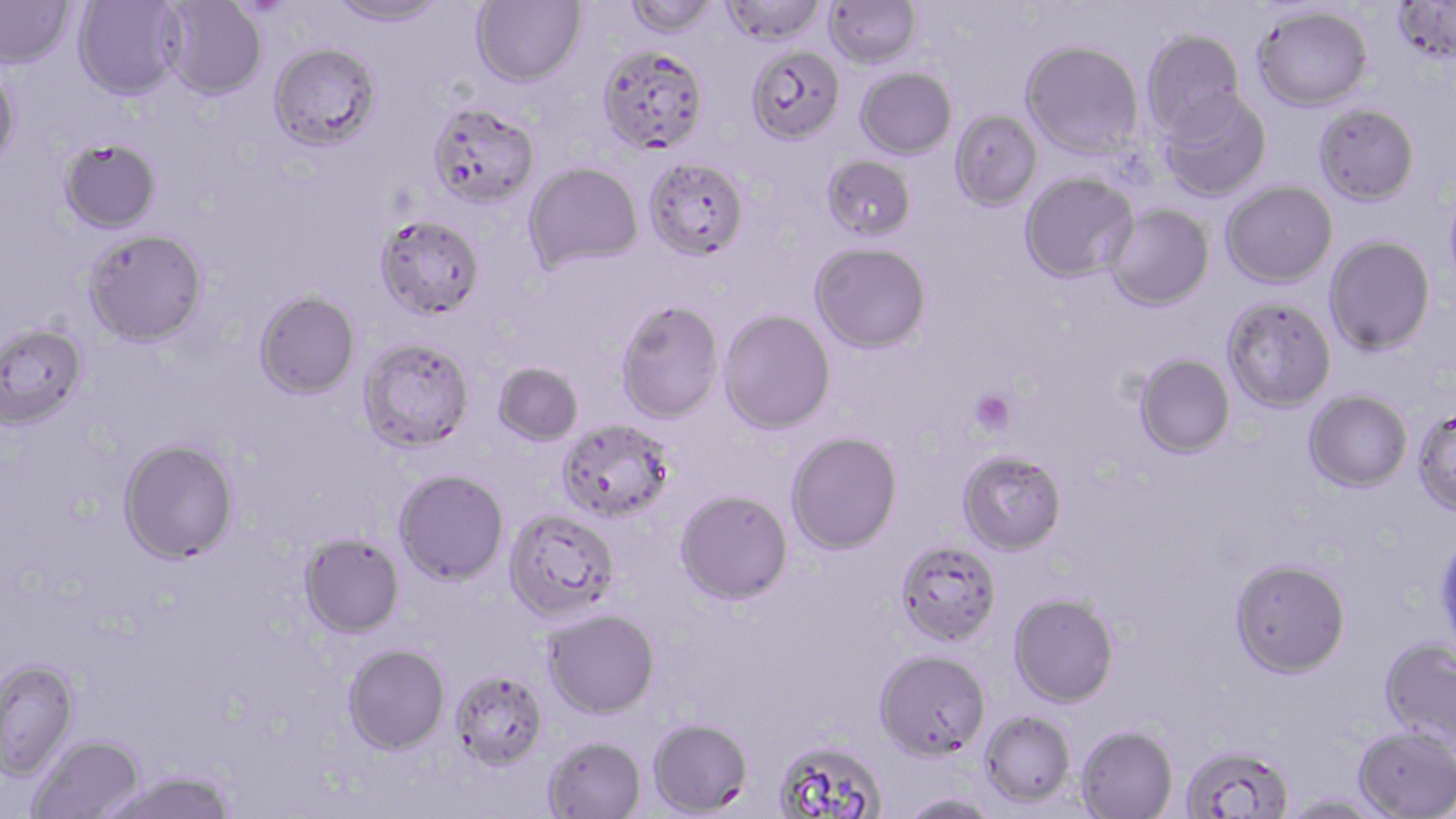
Summary:
  - Coordinate format: approximate bounding boxes as (x1,y1)-(x2,y2) corner pairs in pixels
  - Uninfected red blood cell locations: (0,0)-(74,69), (73,0)-(184,100), (327,0)-(451,27), (470,0)-(586,86), (623,0)-(720,37), (720,0)-(827,45), (823,0)-(921,68), (1392,0)-(1456,65), (160,1)-(267,99), (1252,5)-(1373,111), (1141,30)-(1246,138), (1020,40)-(1144,157), (269,42)-(381,150), (597,44)-(709,154), (746,45)-(845,145), (0,65)-(22,171), (855,67)-(957,159), (1157,88)-(1272,201), (427,102)-(540,209), (1314,104)-(1420,205), (949,110)-(1042,211), (59,137)-(162,233), (821,155)-(917,242), (644,156)-(749,261), (524,161)-(643,273), (1019,172)-(1139,283), (1221,181)-(1337,288), (1444,181)-(1456,296), (1104,204)-(1215,310), (375,213)-(485,320), (82,229)-(208,348), (1324,235)-(1436,355), (810,241)-(931,353), (254,291)-(360,400), (1222,297)-(1336,413), (615,300)-(724,423), (719,310)-(836,434), (0,322)-(88,431), (357,338)-(474,454), (1134,354)-(1235,458), (492,362)-(584,446), (1304,390)-(1412,492), (1412,408)-(1456,516), (557,419)-(676,524), (785,431)-(902,555), (118,438)-(240,564), (957,450)-(1067,554), (393,469)-(509,585), (675,490)-(793,604), (504,508)-(620,623), (1435,526)-(1456,661), (298,533)-(405,638), (896,540)-(1003,646), (1229,558)-(1351,677), (1008,592)-(1119,707), (543,609)-(660,719), (1379,637)-(1456,748), (343,644)-(450,755), (874,648)-(991,760), (0,660)-(80,782), (448,669)-(548,770), (980,710)-(1076,807), (648,718)-(753,816), (1076,725)-(1178,818), (1353,726)-(1456,818), (29,735)-(146,818), (543,735)-(646,818), (774,740)-(887,819), (1179,743)-(1293,819), (101,772)-(237,819), (900,793)-(1004,819), (1281,795)-(1392,818)
  - Platelet locations: (969,389)-(1016,435)
  - Slide-level diagnosis: Plasmodium falciparum
  - Modality: optical microscopy
  - Magnification: 1000x
  - Stain: May-Grünwald-Giemsa
  - Field of view: one of a larger specimen
  - Preparation: thin blood smear
  - Image size: 1456×819 pixels